Assess this cell for malaria.
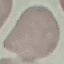
It is uninfected.

Giemsa-stained preparation. Acquired by smartphone through the microscope eyepiece. Thin blood film. Cell patch, automatically extracted from a larger field of view and resized to 64 × 64 pixels.